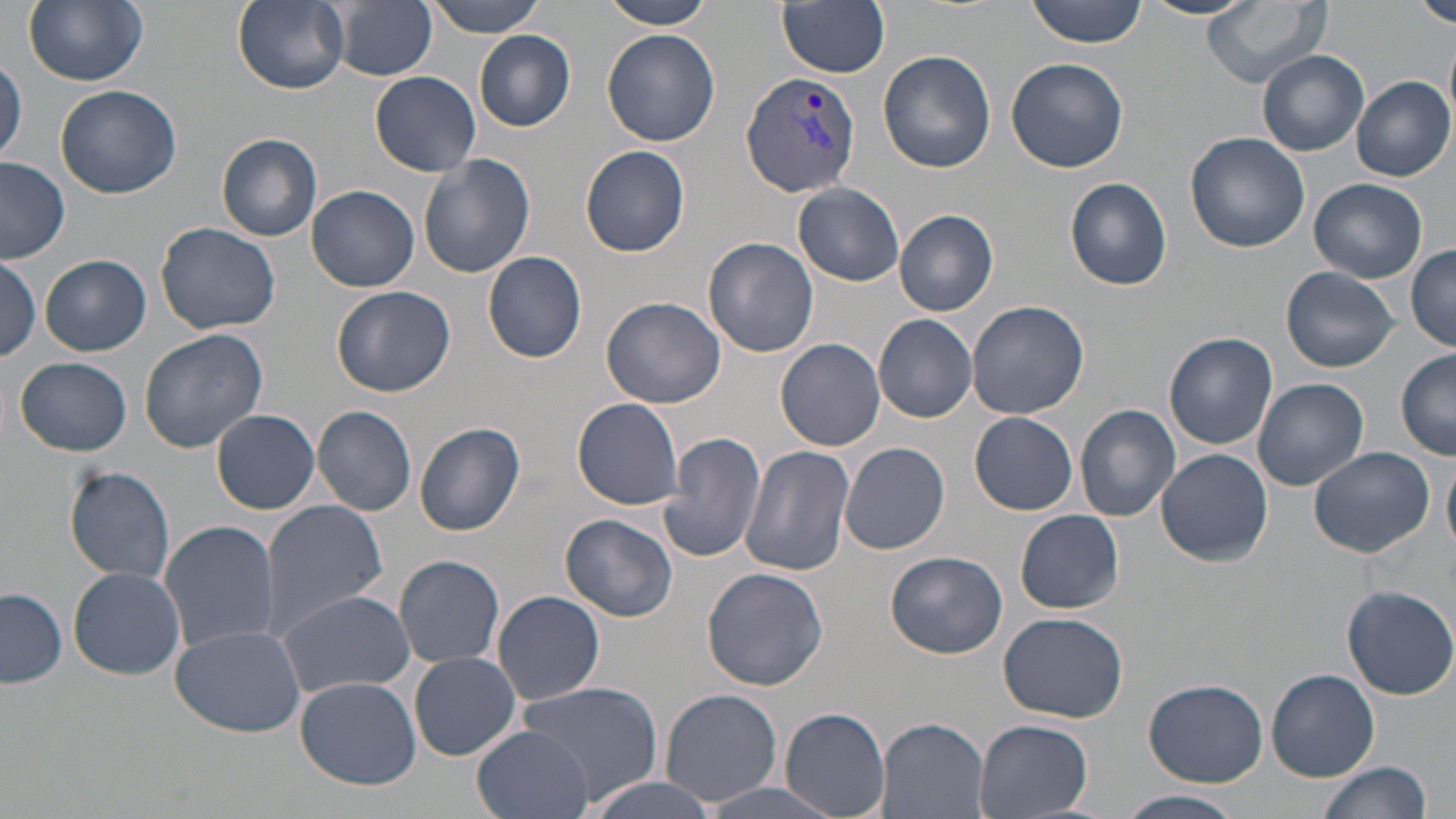
{
  "plasmodium_vivax_infected_red_blood_cell_locations": "approximate bounding boxes as named x1/y1/x2/y2 corners in pixels: (x1=742, y1=70, x2=863, y2=198)",
  "slide_level_diagnosis": "Plasmodium vivax",
  "uninfected_red_blood_cell_locations": "approximate bounding boxes as named x1/y1/x2/y2 corners in pixels: (x1=21, y1=0, x2=149, y2=88), (x1=423, y1=0, x2=553, y2=36), (x1=599, y1=0, x2=719, y2=29), (x1=776, y1=0, x2=890, y2=78), (x1=1028, y1=0, x2=1148, y2=47), (x1=1137, y1=0, x2=1257, y2=20), (x1=1202, y1=0, x2=1331, y2=88), (x1=1416, y1=0, x2=1456, y2=30), (x1=234, y1=1, x2=350, y2=93), (x1=331, y1=1, x2=438, y2=81), (x1=602, y1=28, x2=721, y2=147), (x1=475, y1=30, x2=576, y2=132), (x1=878, y1=48, x2=997, y2=174), (x1=1258, y1=51, x2=1368, y2=157), (x1=1, y1=53, x2=26, y2=167), (x1=1005, y1=56, x2=1128, y2=173), (x1=371, y1=71, x2=481, y2=176), (x1=1350, y1=76, x2=1455, y2=182), (x1=55, y1=84, x2=183, y2=199), (x1=1184, y1=131, x2=1310, y2=253), (x1=216, y1=133, x2=323, y2=241), (x1=578, y1=144, x2=690, y2=257), (x1=418, y1=155, x2=536, y2=278), (x1=0, y1=158, x2=70, y2=264), (x1=1066, y1=176, x2=1173, y2=291), (x1=1310, y1=178, x2=1427, y2=283), (x1=793, y1=183, x2=905, y2=284), (x1=307, y1=185, x2=420, y2=292), (x1=894, y1=210, x2=998, y2=316), (x1=156, y1=222, x2=281, y2=335), (x1=702, y1=236, x2=819, y2=357), (x1=1407, y1=243, x2=1456, y2=351), (x1=483, y1=250, x2=588, y2=363), (x1=41, y1=255, x2=150, y2=356), (x1=0, y1=256, x2=42, y2=363), (x1=1282, y1=267, x2=1398, y2=372), (x1=332, y1=285, x2=456, y2=397), (x1=601, y1=295, x2=728, y2=408), (x1=966, y1=300, x2=1090, y2=421), (x1=873, y1=314, x2=977, y2=422), (x1=139, y1=329, x2=269, y2=453), (x1=1164, y1=332, x2=1277, y2=450), (x1=777, y1=338, x2=886, y2=452), (x1=1397, y1=347, x2=1456, y2=459), (x1=14, y1=356, x2=132, y2=455), (x1=1253, y1=377, x2=1369, y2=491), (x1=572, y1=398, x2=686, y2=511), (x1=1075, y1=403, x2=1181, y2=522), (x1=312, y1=404, x2=418, y2=516), (x1=212, y1=409, x2=322, y2=515), (x1=195, y1=411, x2=309, y2=597), (x1=970, y1=413, x2=1078, y2=514), (x1=414, y1=423, x2=526, y2=537), (x1=659, y1=431, x2=766, y2=563), (x1=840, y1=441, x2=950, y2=554), (x1=739, y1=445, x2=855, y2=576), (x1=1308, y1=446, x2=1437, y2=560), (x1=1156, y1=448, x2=1273, y2=567), (x1=1442, y1=455, x2=1456, y2=558), (x1=64, y1=466, x2=175, y2=584), (x1=257, y1=500, x2=389, y2=638), (x1=1015, y1=509, x2=1124, y2=613), (x1=561, y1=513, x2=678, y2=622), (x1=159, y1=520, x2=279, y2=653), (x1=885, y1=549, x2=1007, y2=659), (x1=394, y1=555, x2=504, y2=670), (x1=69, y1=567, x2=186, y2=680), (x1=701, y1=567, x2=829, y2=691), (x1=1343, y1=584, x2=1456, y2=699), (x1=276, y1=588, x2=415, y2=699), (x1=0, y1=589, x2=66, y2=688), (x1=493, y1=590, x2=605, y2=706), (x1=998, y1=611, x2=1129, y2=723), (x1=171, y1=624, x2=305, y2=738), (x1=409, y1=651, x2=522, y2=762), (x1=1267, y1=668, x2=1380, y2=780), (x1=296, y1=677, x2=420, y2=788), (x1=512, y1=679, x2=664, y2=803), (x1=1143, y1=679, x2=1267, y2=786), (x1=658, y1=688, x2=784, y2=807), (x1=780, y1=706, x2=891, y2=819), (x1=876, y1=716, x2=990, y2=819), (x1=973, y1=719, x2=1092, y2=819), (x1=473, y1=727, x2=591, y2=819), (x1=1316, y1=760, x2=1434, y2=819), (x1=579, y1=774, x2=724, y2=819), (x1=701, y1=779, x2=848, y2=819), (x1=1121, y1=790, x2=1242, y2=819)",
  "preparation": "thin blood smear",
  "magnification": "1000x",
  "image_size": "1456×819 pixels",
  "stain": "May-Grünwald-Giemsa",
  "field_of_view": "one of a larger specimen",
  "modality": "optical microscopy"
}